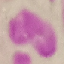

Result: no malaria parasites detected. Photographed with a smartphone camera at the microscope eyepiece. Thin blood smear. Cell patch, automatically extracted from a larger field of view and resized to 64 × 64 pixels. Giemsa stain.